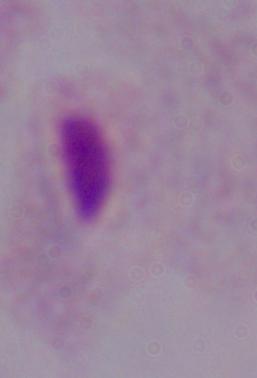
magnification: 1000x
modality: micrograph
identification: trichomonad